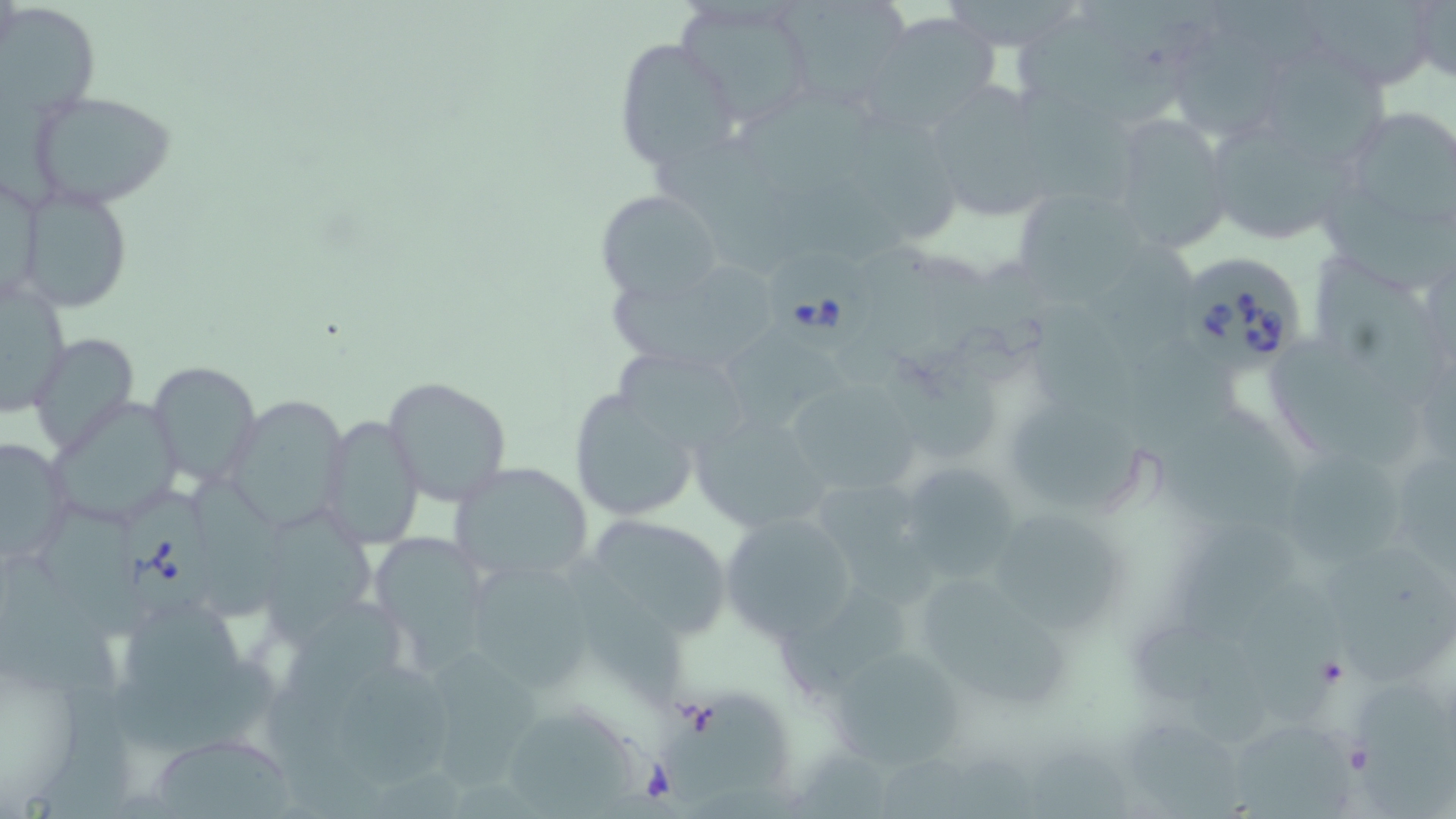
Summary:
  - Coordinate format: approximate bounding boxes as [x1, y1, x2, y2] in pixels
  - Uninfected red blood cell locations: [675, 0, 815, 126], [781, 0, 911, 105], [1289, 1, 1447, 91], [3, 6, 99, 119], [863, 14, 1008, 130], [1016, 22, 1183, 126], [610, 37, 737, 171], [1170, 39, 1286, 143], [1268, 45, 1389, 163], [919, 80, 1055, 220], [27, 90, 175, 208], [846, 108, 956, 236], [1356, 108, 1456, 220], [1104, 111, 1232, 252], [1213, 127, 1356, 245], [17, 183, 135, 314], [1322, 184, 1456, 288], [1020, 186, 1147, 305], [597, 191, 723, 302], [1317, 257, 1443, 406], [612, 262, 775, 379], [0, 277, 71, 417], [1031, 295, 1131, 430], [729, 328, 856, 423], [28, 332, 139, 457], [1270, 339, 1425, 475], [883, 346, 997, 460], [618, 353, 747, 441], [149, 360, 261, 490], [384, 376, 511, 504], [781, 381, 926, 495], [568, 389, 702, 526], [223, 393, 347, 534], [50, 397, 188, 527], [1007, 400, 1149, 511], [1170, 405, 1300, 523], [687, 410, 831, 535], [321, 414, 424, 553], [0, 435, 72, 565], [1282, 449, 1401, 564], [1405, 452, 1456, 573], [450, 462, 595, 586], [917, 471, 1016, 578], [194, 473, 288, 614], [820, 480, 938, 597], [999, 506, 1123, 631], [39, 510, 147, 637], [270, 511, 377, 641], [718, 511, 859, 642], [601, 520, 724, 636], [1179, 520, 1298, 639], [371, 536, 485, 667], [1331, 538, 1454, 685], [570, 557, 683, 710], [475, 566, 592, 691], [920, 580, 1072, 709], [779, 581, 917, 692], [1248, 586, 1341, 719], [280, 598, 408, 709], [125, 602, 247, 718], [1136, 626, 1274, 740], [822, 641, 972, 776], [436, 642, 539, 792], [334, 668, 452, 789], [1356, 680, 1456, 819], [663, 693, 792, 806], [510, 714, 644, 819], [1136, 718, 1243, 819], [1236, 721, 1352, 819], [160, 740, 294, 819], [1032, 748, 1135, 819]
  - Babesia divergens-infected red blood cell locations: [773, 253, 872, 356], [1181, 257, 1300, 376], [122, 495, 224, 615]
  - Slide-level diagnosis: Babesia divergens
  - Modality: optical microscopy
  - Magnification: 1000x
  - Image size: 1456×819 pixels
  - Field of view: one of a larger specimen
  - Stain: May-Grünwald-Giemsa
  - Preparation: thin blood smear